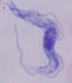 A trypanosome is seen. 1000x magnification. Micrograph.